Comment on the morphology of the red blood cells.
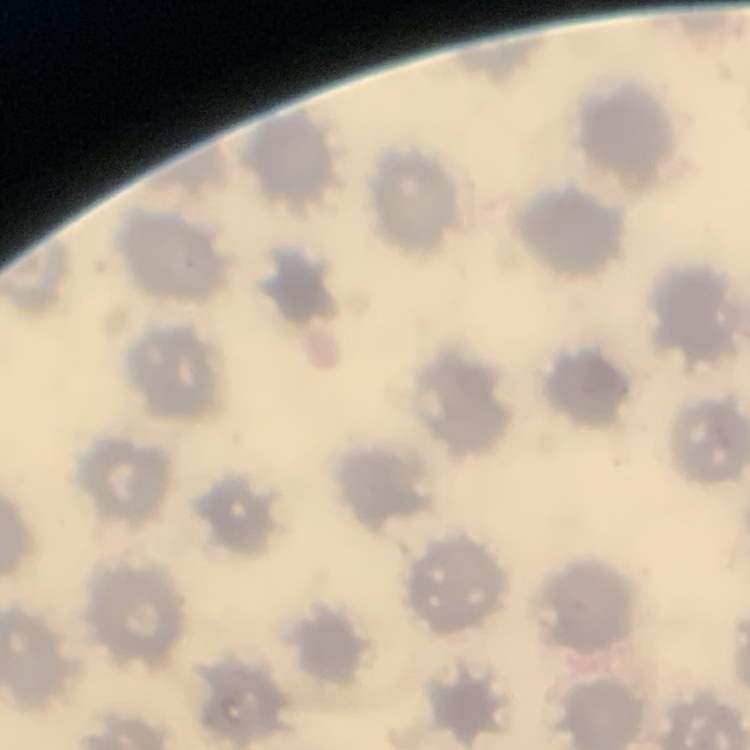

No rouleaux formation.

Summary:
  - Stain: Field's or Giemsa
  - Image type: square crop of a larger photomicrograph
  - Preparation: thin blood film